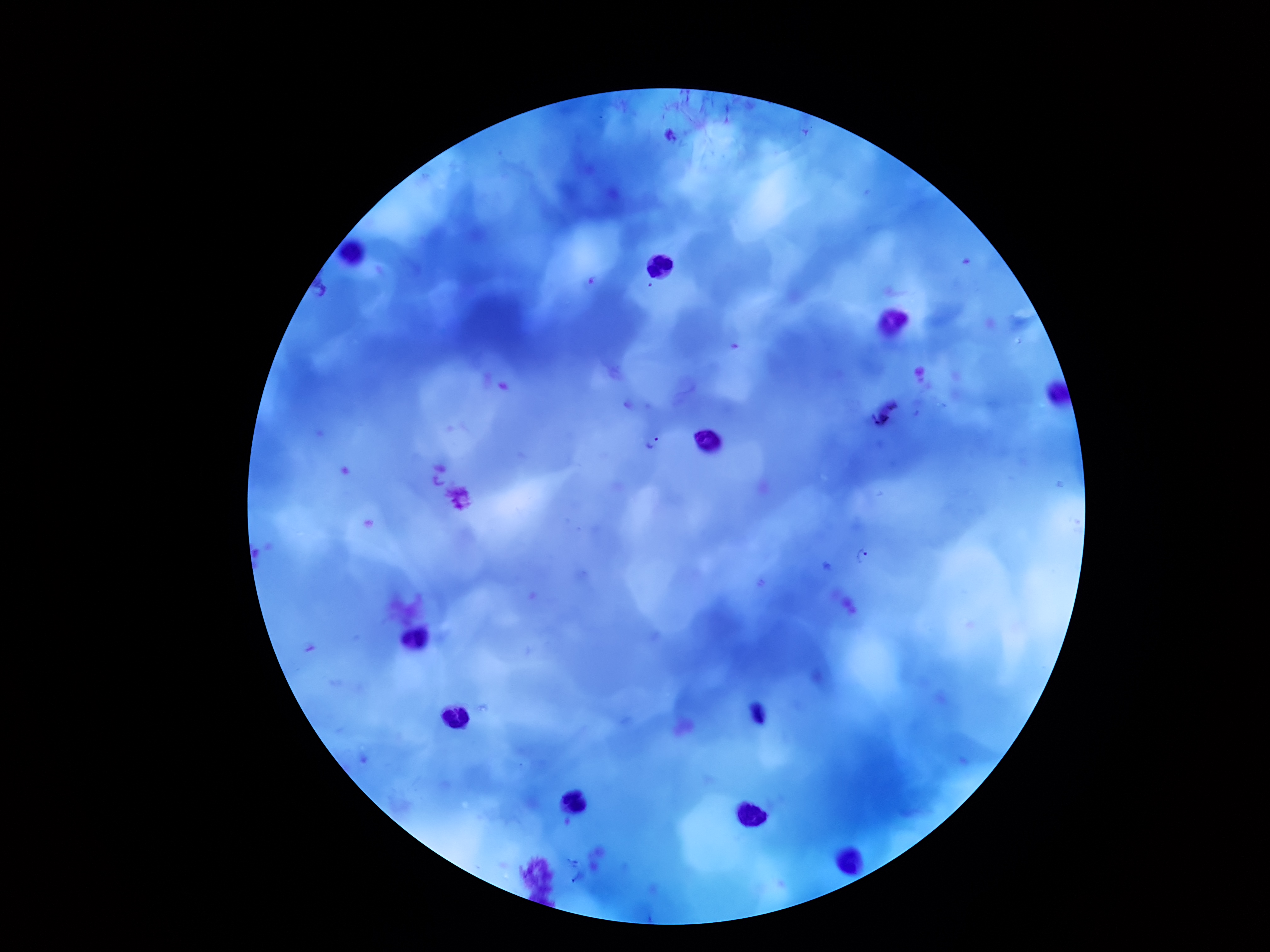
Approximate centers as {x, y} in pixels.
Summary:
  - Plasmodium parasite locations: {651, 445}, {866, 560}
  - Capture: smartphone camera through the microscope eyepiece
  - Image size: 1270×952 pixels
  - Field of view: single
  - Patient malaria status: positive
  - Magnification: 100x
  - Preparation: thick blood film
  - Stain: Giemsa